Report the malaria status of this cell.
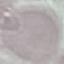
Uninfected.

Summary:
  - Preparation: thin smear
  - Stain: Giemsa
  - Image type: cell patch, automatically extracted from a larger field of view and resized to 64 × 64 pixels
  - Capture: smartphone through the microscope eyepiece